State the blood parasite species.
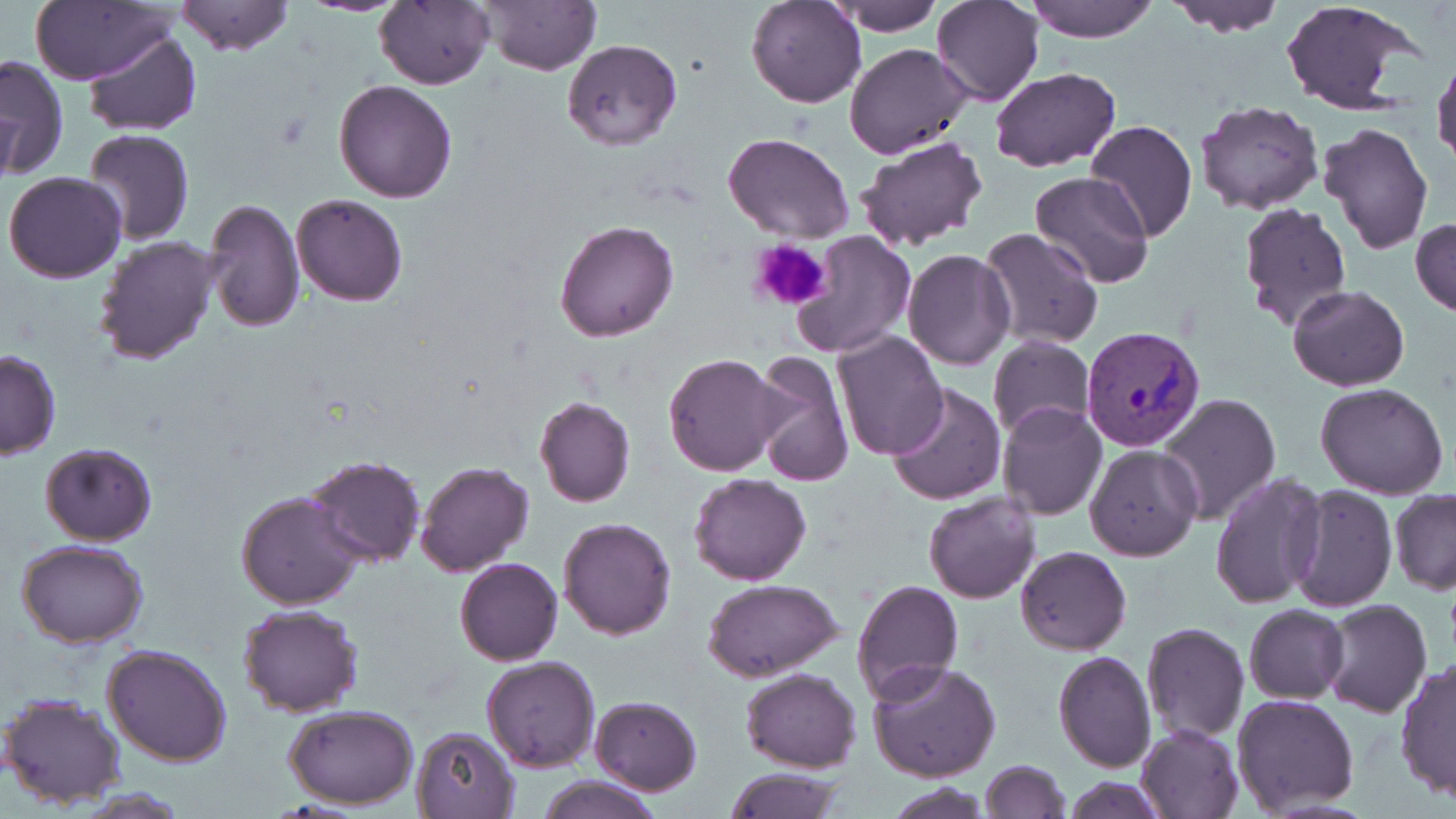

Plasmodium vivax.

magnification = 1000x
uninfected red blood cell locations = approximate bounding boxes as named x1/y1/x2/y2 corners in pixels: (x1=27, y1=0, x2=177, y2=86), (x1=174, y1=0, x2=293, y2=55), (x1=296, y1=0, x2=411, y2=14), (x1=374, y1=0, x2=495, y2=90), (x1=479, y1=0, x2=601, y2=74), (x1=745, y1=0, x2=867, y2=108), (x1=932, y1=0, x2=1043, y2=107), (x1=1026, y1=0, x2=1161, y2=41), (x1=1166, y1=0, x2=1288, y2=36), (x1=1279, y1=0, x2=1428, y2=115), (x1=831, y1=1, x2=941, y2=35), (x1=82, y1=30, x2=202, y2=136), (x1=560, y1=38, x2=683, y2=153), (x1=844, y1=43, x2=972, y2=158), (x1=1433, y1=53, x2=1455, y2=172), (x1=0, y1=54, x2=67, y2=178), (x1=990, y1=70, x2=1117, y2=170), (x1=333, y1=80, x2=458, y2=202), (x1=1195, y1=101, x2=1324, y2=213), (x1=1087, y1=114, x2=1315, y2=234), (x1=1085, y1=120, x2=1197, y2=242), (x1=1317, y1=120, x2=1433, y2=253), (x1=82, y1=129, x2=194, y2=244), (x1=722, y1=131, x2=854, y2=242), (x1=855, y1=135, x2=988, y2=252), (x1=3, y1=171, x2=126, y2=283), (x1=1028, y1=171, x2=1155, y2=288), (x1=291, y1=193, x2=408, y2=307), (x1=205, y1=198, x2=304, y2=334), (x1=1238, y1=201, x2=1352, y2=328), (x1=1411, y1=218, x2=1455, y2=317), (x1=552, y1=219, x2=678, y2=340), (x1=978, y1=227, x2=1105, y2=352), (x1=790, y1=232, x2=916, y2=359), (x1=92, y1=236, x2=223, y2=364), (x1=902, y1=248, x2=1016, y2=370), (x1=1287, y1=283, x2=1410, y2=392), (x1=832, y1=332, x2=948, y2=460), (x1=988, y1=336, x2=1095, y2=440), (x1=0, y1=349, x2=60, y2=459), (x1=664, y1=353, x2=788, y2=476), (x1=750, y1=353, x2=854, y2=488), (x1=1314, y1=382, x2=1449, y2=500), (x1=886, y1=383, x2=1007, y2=506), (x1=1157, y1=391, x2=1283, y2=527), (x1=535, y1=395, x2=635, y2=507), (x1=998, y1=402, x2=1107, y2=519), (x1=39, y1=442, x2=157, y2=545), (x1=1083, y1=445, x2=1203, y2=561), (x1=303, y1=455, x2=427, y2=569), (x1=413, y1=460, x2=534, y2=576), (x1=1209, y1=472, x2=1330, y2=612), (x1=688, y1=473, x2=813, y2=586), (x1=1287, y1=482, x2=1395, y2=612), (x1=921, y1=490, x2=1040, y2=604), (x1=1389, y1=490, x2=1456, y2=595), (x1=236, y1=491, x2=366, y2=608), (x1=558, y1=516, x2=676, y2=640), (x1=17, y1=539, x2=148, y2=648), (x1=1015, y1=545, x2=1132, y2=655), (x1=454, y1=557, x2=562, y2=665), (x1=850, y1=577, x2=964, y2=706), (x1=702, y1=579, x2=845, y2=680), (x1=1320, y1=598, x2=1432, y2=718), (x1=237, y1=603, x2=363, y2=717), (x1=1243, y1=603, x2=1349, y2=704), (x1=1141, y1=621, x2=1250, y2=744), (x1=102, y1=643, x2=233, y2=767), (x1=1052, y1=649, x2=1156, y2=772), (x1=480, y1=655, x2=600, y2=773), (x1=1395, y1=659, x2=1455, y2=799), (x1=868, y1=661, x2=1003, y2=783), (x1=740, y1=667, x2=862, y2=773), (x1=2, y1=692, x2=127, y2=808), (x1=1232, y1=693, x2=1361, y2=814), (x1=589, y1=695, x2=703, y2=794), (x1=282, y1=704, x2=419, y2=809), (x1=1134, y1=724, x2=1243, y2=819), (x1=410, y1=725, x2=519, y2=819), (x1=979, y1=758, x2=1069, y2=818), (x1=721, y1=766, x2=846, y2=819), (x1=535, y1=774, x2=665, y2=819), (x1=1065, y1=777, x2=1169, y2=818)
Plasmodium vivax-infected red blood cell locations = approximate bounding boxes as named x1/y1/x2/y2 corners in pixels: (x1=1080, y1=324, x2=1205, y2=451)
stain = May-Grünwald-Giemsa
preparation = thin blood smear
modality = light microscopy
field of view = one of a larger specimen
platelet locations = approximate bounding boxes as named x1/y1/x2/y2 corners in pixels: (x1=750, y1=239, x2=832, y2=314)
image size = 1456×819 pixels